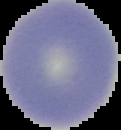
{
  "malaria_status": "uninfected",
  "preparation": "thin blood smear",
  "image_size": "121×130 pixels",
  "image_type": "cell region segmented out of the field of view; surrounding area masked to black"
}